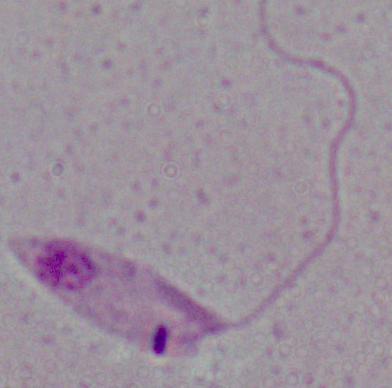 1000x magnification. Photomicrograph. A Leishmania parasite is shown.